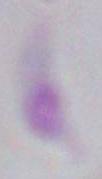

magnification = 1000x
modality = micrograph
identification = Toxoplasma gondii